Describe the morphology of the red blood cells.
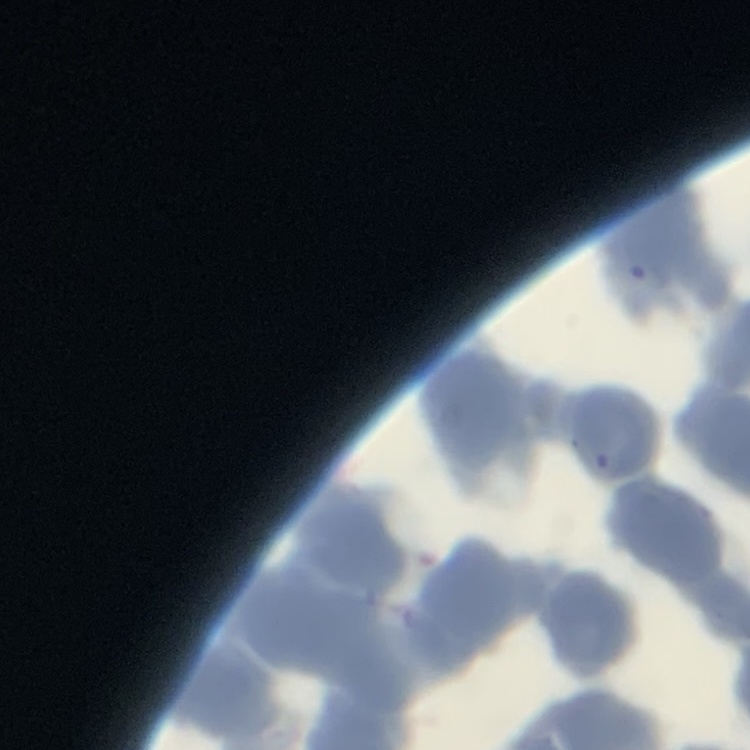
Rouleaux formation.

{
  "stain": "Field's or Giemsa",
  "image_type": "square crop of a larger photomicrograph",
  "preparation": "thin blood film"
}